Give the position of every leukocyte visible.
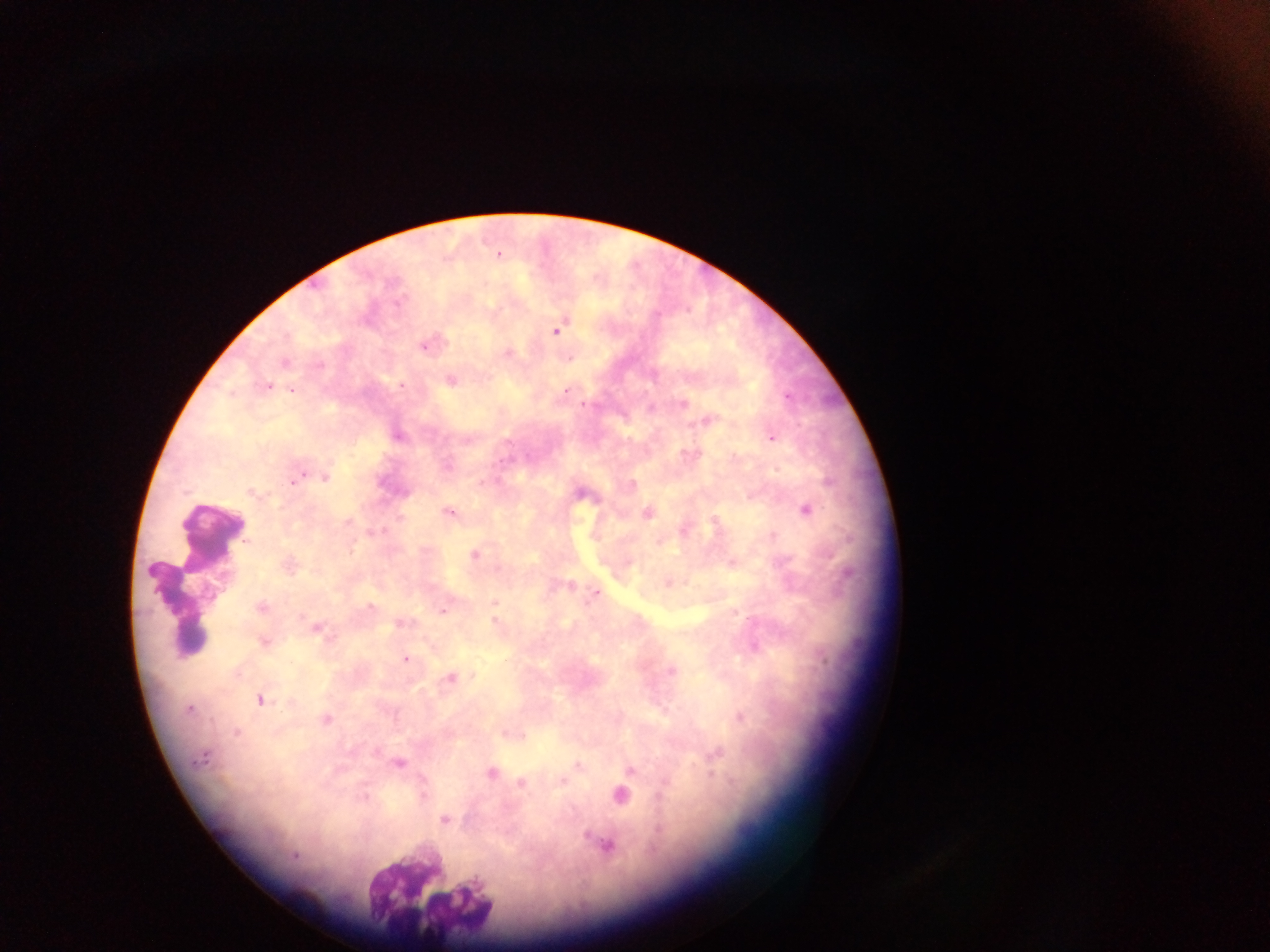

Approximate centers as (x, y) in pixels.
Leukocytes: (196, 584), (424, 887).

Summary:
  - Malaria parasite locations: (499, 255), (398, 305), (555, 330), (445, 342), (423, 344), (430, 344), (505, 353), (449, 378), (401, 385), (268, 386), (565, 391), (789, 394), (684, 403), (583, 405), (652, 407), (705, 422), (696, 423), (399, 437), (771, 437), (464, 442), (684, 455), (448, 465), (304, 471), (296, 473), (325, 477), (289, 484), (631, 484), (249, 493), (806, 511), (449, 512), (648, 513), (399, 519), (346, 521), (239, 525), (384, 531), (773, 535), (351, 546), (473, 554), (730, 562), (151, 572), (671, 582), (572, 584), (553, 587), (593, 594), (493, 602), (371, 606), (260, 607), (442, 610), (733, 613), (737, 616), (495, 621), (398, 624), (318, 629), (331, 639), (262, 643), (405, 660), (672, 670), (450, 677), (259, 700), (288, 702), (191, 708), (738, 716), (325, 721), (505, 732), (235, 733), (522, 735), (376, 752), (717, 752), (206, 756), (199, 760), (399, 764), (577, 765), (630, 772), (490, 773), (711, 776), (562, 781), (520, 784), (664, 784), (618, 796), (424, 797), (444, 821), (656, 827), (584, 835), (608, 847), (294, 857)
  - Capture: mobile-phone photograph through a microscope
  - Country: Ghana
  - Field of view: single
  - Image size: 1270×952 pixels
  - Preparation: thick blood film